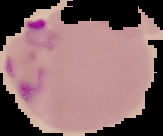

malaria status = parasitized
image size = 163×136 pixels
image type = segmented cell region with the area outside set to black
preparation = thin blood film